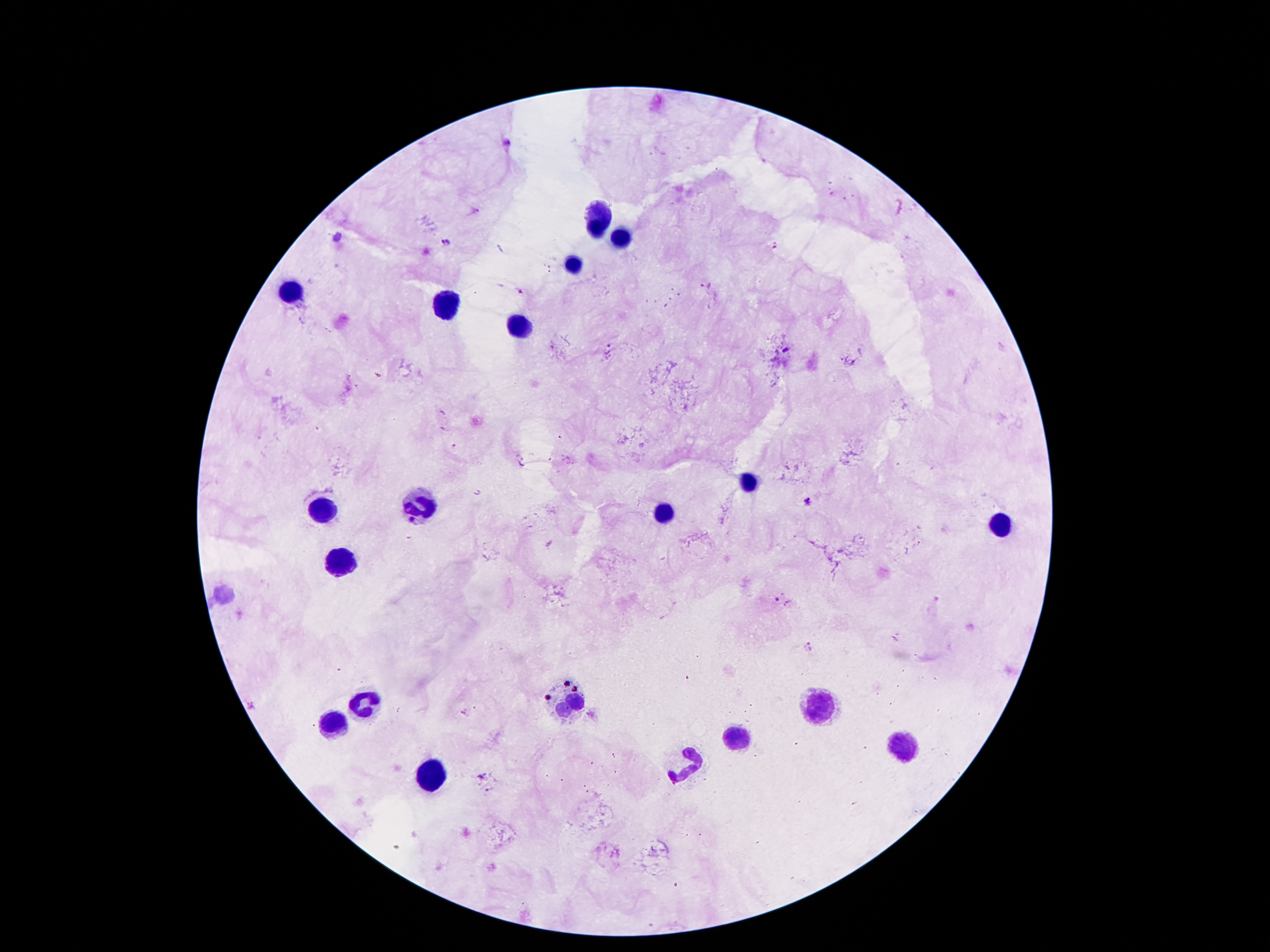

Approximate centers as {x, y} in pixels.
Summary:
  - Leukocyte locations: {597, 218}, {624, 238}, {574, 266}, {295, 293}, {447, 304}, {519, 327}, {749, 481}, {422, 499}, {322, 506}, {665, 511}, {994, 524}, {338, 563}, {365, 701}, {565, 704}, {819, 704}, {335, 724}, {733, 740}, {905, 745}, {685, 760}, {426, 776}
  - Plasmodium parasite locations: {507, 143}, {447, 243}, {521, 292}, {785, 348}, {808, 499}, {778, 598}, {809, 646}, {465, 714}, {481, 776}
  - Stain: Giemsa
  - Patient malaria status: infected with Plasmodium falciparum
  - Field of view: one from this slide
  - Magnification: 100x
  - Capture: smartphone camera through the microscope eyepiece
  - Image size: 1270×952 pixels
  - Preparation: thick peripheral-blood smear